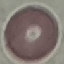

malaria_status: uninfected
stain: Giemsa
capture: smartphone through the microscope eyepiece
image_type: automatically extracted cell patch, resized to 64 × 64 pixels
preparation: thin blood smear